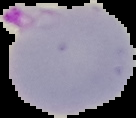

{
  "malaria_status": "parasitized",
  "preparation": "thin blood smear",
  "image_size": "136×118 pixels",
  "image_type": "segmented cell region with the area outside set to black"
}